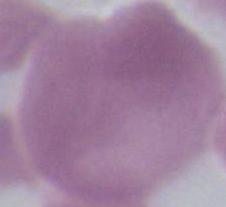

{
  "identification": "red blood cell",
  "modality": "photomicrograph",
  "magnification": "1000x"
}